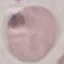
result = no malaria parasites detected
preparation = thin blood film
stain = Giemsa
image type = cell patch, automatically extracted from a larger field of view and resized to 64 × 64 pixels
capture = smartphone camera at the microscope eyepiece